Name the parasite shown.
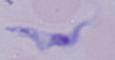

A trypanosome.

Summary:
  - Modality: photomicrograph
  - Magnification: 1000x